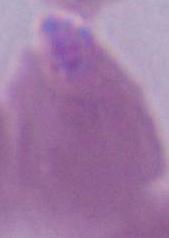

Summary:
  - Identification: erythrocyte
  - Magnification: 1000x
  - Modality: micrograph